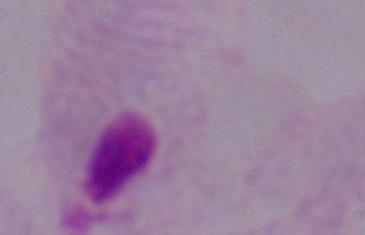
Summary:
  - Magnification: 1000x
  - Identification: trichomonad
  - Modality: micrograph